Name the parasite shown.
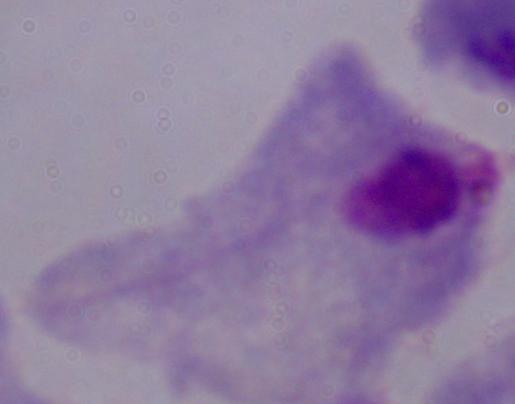

A trichomonad.

Summary:
  - Magnification: 1000x
  - Modality: photomicrograph